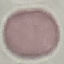
result = no malaria parasites detected
stain = Giemsa
capture = smartphone camera at the microscope eyepiece
preparation = thin blood smear
image type = automatically extracted cell patch, resized to 64 × 64 pixels